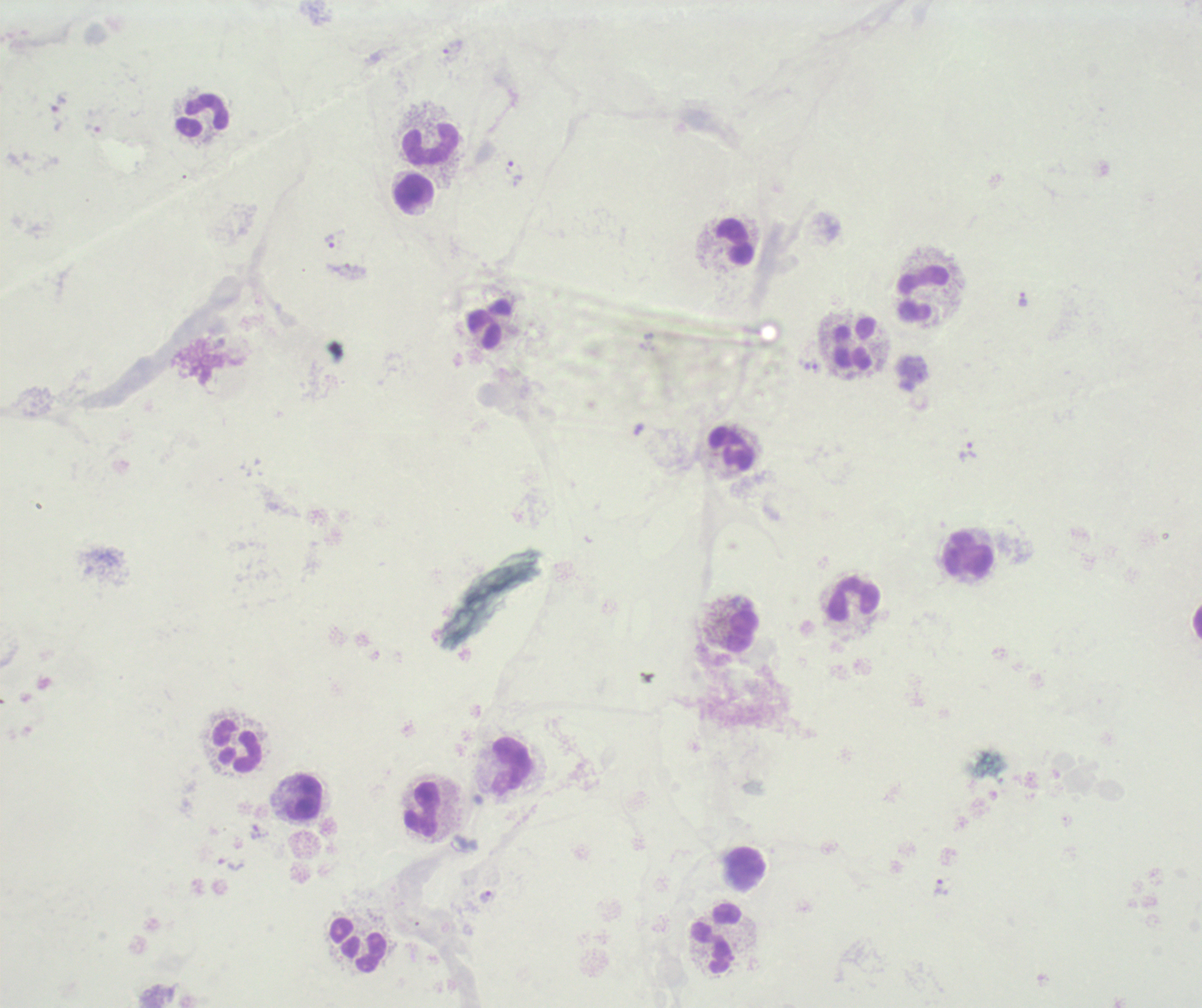
Approximate object centers, in pixels from the top-left corner. Leukocyte locations: (x=204, y=116), (x=431, y=145), (x=413, y=193), (x=735, y=240), (x=923, y=296), (x=490, y=325), (x=853, y=346), (x=732, y=449), (x=968, y=554), (x=854, y=599), (x=741, y=631), (x=237, y=746), (x=510, y=765), (x=305, y=799), (x=422, y=809), (x=744, y=871), (x=716, y=940), (x=357, y=945). Trophozoite locations: (x=453, y=46), (x=59, y=104), (x=509, y=167), (x=330, y=241), (x=1023, y=299), (x=810, y=367), (x=967, y=451), (x=231, y=864), (x=941, y=888), (x=485, y=897). Image is 1202×1008 pixels. Previously used in a real diagnosis. 100x magnification. One field from this slide. Thick smear of blood. Background quality: unsatisfactory. Result: positive for malaria parasites. Romanowsky-stained preparation.